Outline platelets.
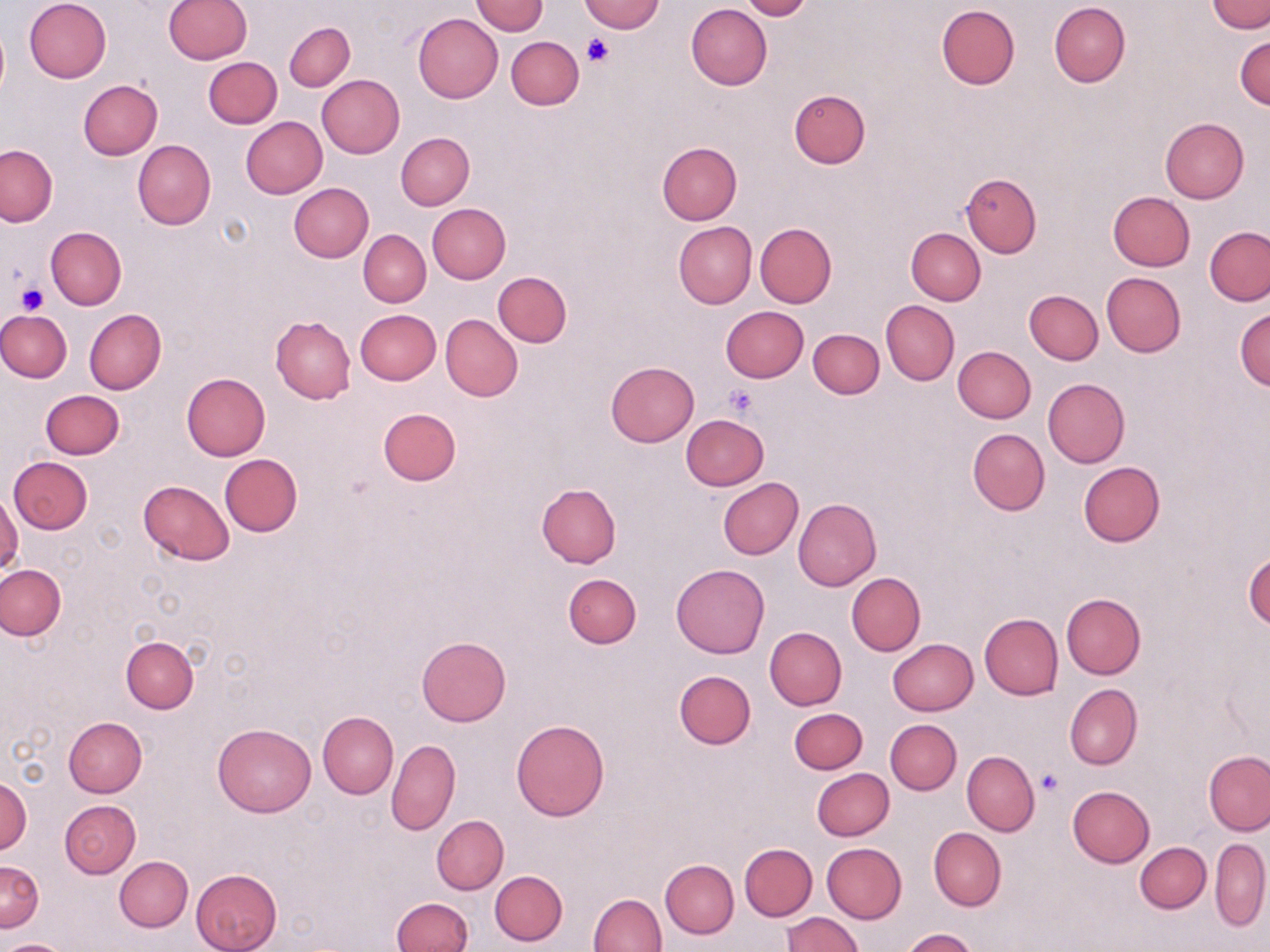
Approximate bounding boxes as [x1, y1, x2, y2] in pixels.
Platelets: [584, 35, 614, 65], [14, 283, 49, 316], [725, 384, 758, 416], [1037, 769, 1064, 796].

Summary:
  - Uninfected red blood cell locations: [24, 0, 110, 83], [164, 0, 251, 64], [577, 0, 664, 33], [739, 0, 815, 20], [471, 1, 548, 36], [1207, 1, 1270, 33], [1049, 2, 1130, 88], [685, 4, 772, 89], [936, 4, 1020, 91], [412, 14, 503, 102], [283, 21, 355, 91], [1235, 34, 1270, 110], [506, 36, 583, 110], [203, 57, 281, 128], [316, 75, 404, 158], [77, 80, 163, 160], [789, 89, 870, 170], [241, 116, 327, 198], [1160, 117, 1249, 202], [396, 132, 474, 210], [132, 140, 216, 230], [656, 142, 742, 224], [0, 145, 57, 226], [961, 173, 1042, 257], [289, 182, 373, 262], [1107, 191, 1195, 271], [427, 203, 510, 283], [674, 222, 757, 309], [755, 223, 836, 308], [1204, 225, 1270, 306], [45, 226, 127, 309], [906, 227, 985, 304], [359, 229, 430, 307], [493, 271, 572, 347], [1101, 272, 1186, 357], [1024, 290, 1103, 365], [880, 300, 959, 385], [720, 306, 809, 383], [1234, 308, 1270, 390], [83, 309, 166, 395], [356, 309, 441, 384], [0, 310, 71, 382], [440, 313, 522, 401], [270, 316, 355, 404], [808, 328, 884, 399], [953, 346, 1035, 423], [606, 361, 699, 447], [182, 373, 270, 460], [1043, 377, 1130, 468], [41, 390, 124, 459], [378, 407, 461, 486], [680, 414, 770, 491], [968, 428, 1050, 515], [219, 453, 302, 536], [9, 457, 91, 533], [1078, 462, 1165, 547], [717, 477, 803, 560], [138, 479, 235, 564], [535, 482, 621, 567], [0, 490, 24, 579], [794, 497, 881, 590], [1243, 551, 1270, 632], [671, 563, 770, 659], [0, 564, 66, 639], [846, 572, 925, 656], [564, 573, 642, 648], [1060, 593, 1146, 679], [980, 613, 1063, 699], [765, 627, 846, 709], [417, 634, 510, 725], [120, 636, 199, 713], [887, 638, 978, 715], [889, 641, 967, 793], [674, 670, 755, 749], [1064, 683, 1142, 770], [789, 707, 867, 774], [318, 711, 398, 799], [64, 716, 147, 797], [885, 719, 962, 794], [510, 720, 610, 821], [212, 722, 316, 817], [387, 739, 460, 835], [1204, 750, 1270, 834], [962, 751, 1039, 835], [812, 768, 894, 841], [0, 775, 31, 854], [1067, 785, 1156, 865], [60, 800, 140, 877], [432, 814, 508, 894], [928, 827, 1005, 911], [1209, 839, 1270, 931], [1134, 841, 1211, 913], [821, 842, 907, 923], [740, 843, 817, 921], [115, 856, 193, 932], [660, 859, 738, 938], [0, 860, 42, 932], [191, 868, 282, 952], [490, 870, 568, 945], [590, 893, 666, 952], [393, 898, 473, 952], [783, 913, 863, 952], [901, 928, 979, 952], [2, 940, 71, 952]
  - Slide-level diagnosis: no evidence of blood parasites
  - Preparation: thin blood smear
  - Image size: 1270×952 pixels
  - Modality: optical microscopy
  - Magnification: 1000x
  - Stain: May-Grünwald-Giemsa
  - Field of view: single